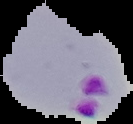
Summary:
  - Preparation: thin blood film
  - Image size: 133×124 pixels
  - Image type: cell region segmented out of the field of view; surrounding area masked to black
  - Malaria status: parasitized